Outline each uninfected red blood cell.
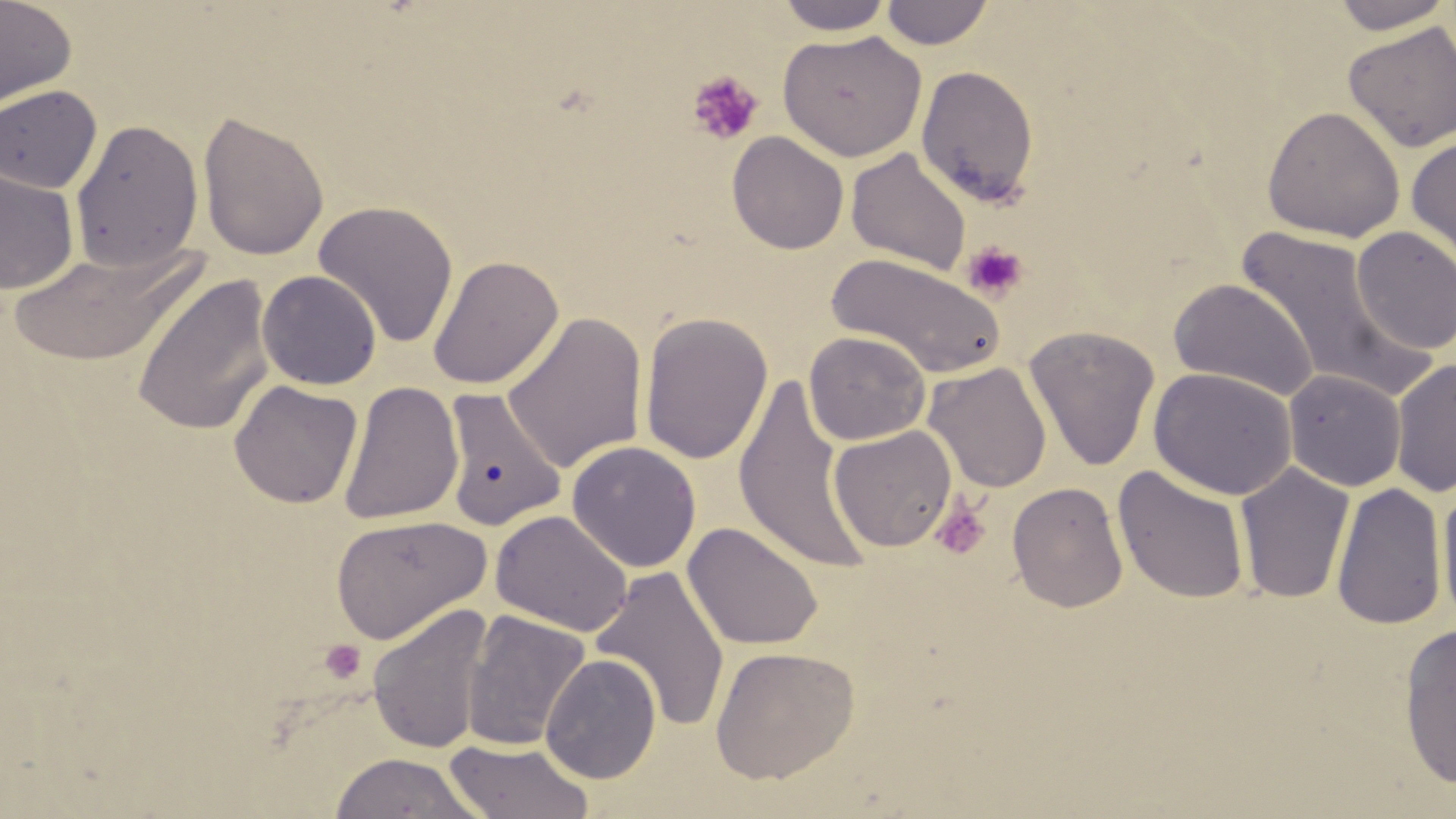
Approximate bounding boxes as [x1, y1, x2, y2] in pixels.
Uninfected red blood cells: [0, 0, 77, 115], [775, 0, 896, 35], [1329, 0, 1455, 34], [881, 1, 994, 49], [1342, 20, 1456, 153], [777, 30, 928, 162], [916, 64, 1039, 208], [0, 84, 102, 194], [1262, 106, 1405, 243], [196, 109, 329, 262], [70, 118, 204, 273], [726, 131, 849, 255], [1406, 136, 1456, 271], [845, 146, 971, 276], [0, 167, 79, 296], [312, 200, 459, 349], [1232, 225, 1429, 401], [1351, 225, 1456, 356], [6, 241, 206, 366], [826, 252, 1007, 378], [427, 254, 564, 389], [257, 270, 382, 390], [132, 273, 275, 437], [1169, 278, 1320, 402], [501, 312, 647, 474], [638, 312, 772, 465], [1024, 326, 1161, 472], [804, 331, 931, 445], [1390, 358, 1456, 498], [923, 361, 1052, 493], [1148, 367, 1298, 500], [1283, 369, 1406, 491], [732, 373, 871, 575], [229, 379, 362, 509], [339, 380, 464, 525], [441, 387, 566, 531], [828, 425, 958, 552], [566, 441, 702, 573], [1234, 462, 1355, 605], [1112, 466, 1251, 604], [1007, 482, 1128, 613], [1331, 482, 1447, 631], [1436, 484, 1456, 630], [490, 509, 633, 637], [330, 514, 490, 645], [683, 522, 824, 652], [590, 565, 731, 734], [367, 602, 494, 755], [462, 610, 591, 752], [1398, 622, 1456, 790], [710, 645, 860, 784], [540, 653, 661, 784], [443, 738, 597, 819], [327, 752, 487, 818].

{
  "slide_level_diagnosis": "no evidence of blood parasites",
  "platelet_locations": "approximate bounding boxes as [x1, y1, x2, y2] in pixels: [687, 71, 763, 145], [962, 240, 1029, 302], [929, 496, 992, 561], [319, 639, 366, 684]",
  "preparation": "thin blood smear",
  "magnification": "1000x",
  "image_size": "1456×819 pixels",
  "modality": "optical microscopy",
  "field_of_view": "one of a larger specimen",
  "stain": "May-Grünwald-Giemsa"
}